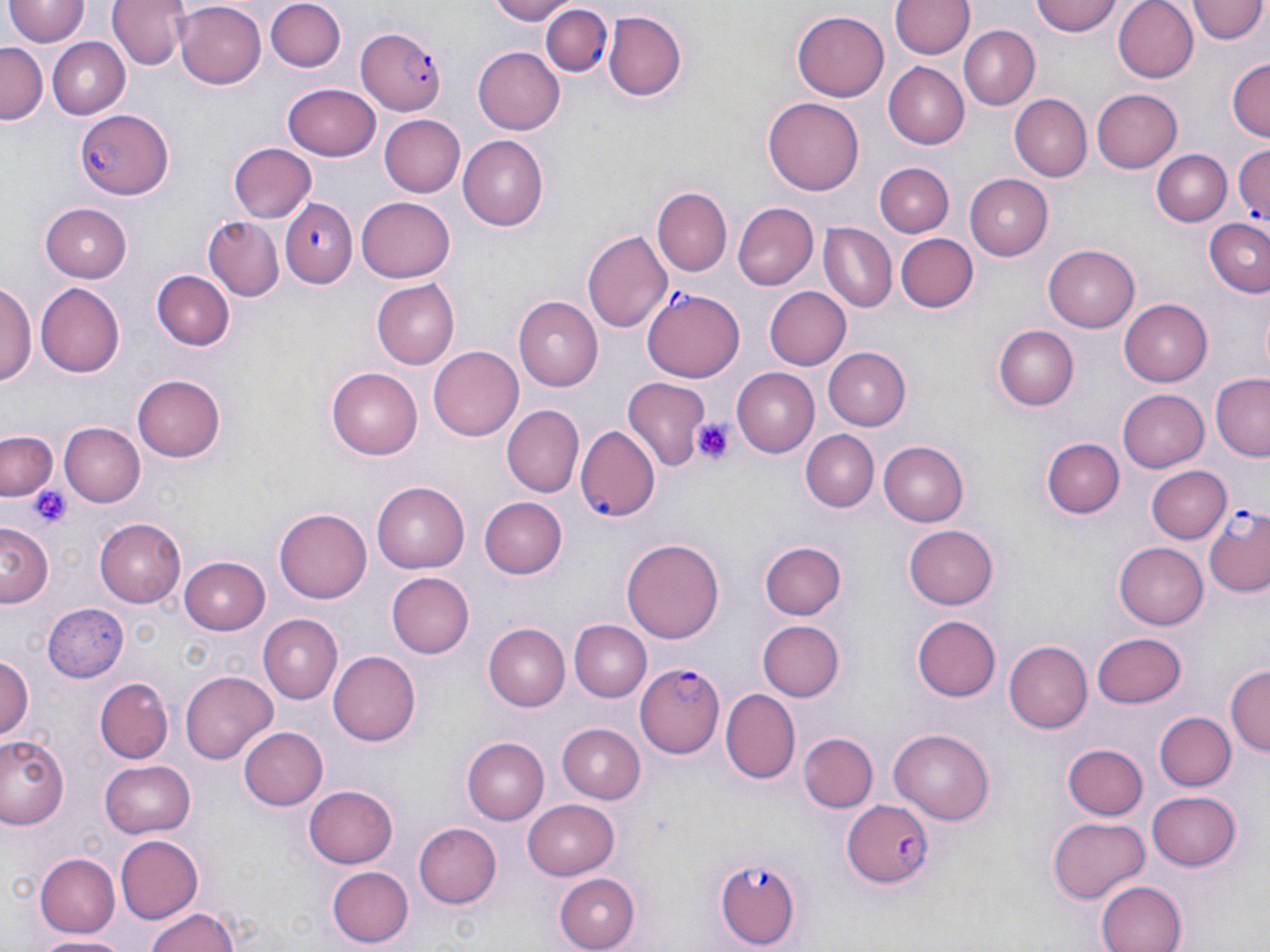

Summary:
  - Coordinate format: approximate bounding boxes as (x1, y1, x2, y2) in pixels
  - Uninfected red blood cell locations: (5, 0, 88, 47), (108, 0, 189, 69), (486, 0, 578, 24), (893, 0, 973, 60), (1030, 0, 1123, 37), (1111, 0, 1198, 83), (174, 2, 267, 88), (267, 2, 342, 73), (1189, 2, 1268, 47), (794, 8, 892, 102), (602, 10, 685, 102), (960, 27, 1039, 110), (46, 36, 129, 117), (0, 43, 46, 123), (472, 46, 565, 134), (1227, 58, 1268, 142), (882, 62, 970, 148), (283, 82, 381, 159), (1092, 89, 1183, 173), (1012, 94, 1093, 180), (763, 97, 865, 195), (377, 114, 464, 197), (457, 136, 550, 231), (229, 142, 318, 223), (1153, 150, 1231, 227), (875, 161, 953, 237), (962, 174, 1053, 259), (652, 186, 732, 276), (357, 194, 456, 281), (42, 202, 134, 280), (733, 202, 818, 289), (1203, 217, 1270, 296), (204, 218, 284, 302), (821, 223, 896, 311), (583, 230, 672, 336), (896, 234, 978, 312), (1044, 246, 1139, 332), (156, 270, 233, 349), (375, 279, 461, 369), (35, 283, 126, 377), (1, 284, 36, 388), (763, 287, 850, 371), (517, 296, 604, 391), (1119, 298, 1212, 385), (994, 325, 1079, 411), (428, 346, 526, 441), (822, 347, 910, 430), (326, 368, 423, 457), (732, 369, 820, 457), (133, 375, 227, 461), (1211, 376, 1269, 460), (624, 379, 710, 472), (1118, 389, 1210, 472), (504, 406, 582, 497), (59, 422, 145, 507), (800, 431, 877, 511), (0, 433, 57, 499), (1043, 437, 1123, 518), (879, 440, 968, 527), (1145, 466, 1230, 544), (373, 480, 470, 573), (480, 496, 569, 579), (275, 507, 372, 601), (96, 518, 188, 607), (2, 525, 51, 609), (903, 525, 999, 609), (621, 537, 726, 644), (759, 540, 846, 620), (1115, 544, 1208, 629), (179, 556, 270, 634), (388, 572, 475, 657), (44, 603, 127, 681), (259, 615, 342, 703), (912, 615, 1001, 702), (756, 619, 844, 702), (568, 620, 651, 702), (484, 624, 570, 710), (1093, 632, 1187, 708), (1006, 639, 1097, 734), (328, 651, 420, 745), (0, 654, 34, 742), (1225, 665, 1269, 759), (180, 671, 277, 763), (96, 676, 173, 762), (722, 688, 800, 784), (1156, 711, 1235, 791), (556, 723, 645, 806), (237, 725, 328, 811), (889, 729, 994, 824), (0, 733, 70, 831), (798, 733, 876, 814), (462, 737, 550, 824), (1063, 743, 1148, 820), (102, 760, 196, 837), (303, 785, 400, 868), (1149, 790, 1243, 869), (523, 799, 619, 878), (1047, 815, 1151, 903), (411, 821, 502, 911), (114, 834, 202, 925), (34, 853, 120, 937), (327, 866, 413, 948), (552, 871, 640, 951), (1093, 878, 1187, 952), (144, 908, 243, 952), (38, 933, 134, 951)
  - Platelet locations: (693, 417, 738, 466), (32, 484, 73, 530)
  - Plasmodium falciparum-infected red blood cell locations: (541, 5, 613, 78), (356, 28, 447, 113), (77, 108, 171, 199), (1234, 142, 1269, 232), (282, 198, 357, 289), (641, 289, 745, 382), (577, 427, 659, 522), (1203, 505, 1270, 598), (636, 660, 739, 757), (842, 799, 936, 888), (715, 856, 801, 950)
  - Slide-level diagnosis: Plasmodium falciparum
  - Stain: May-Grünwald-Giemsa
  - Image size: 1270×952 pixels
  - Field of view: one of a larger specimen
  - Magnification: 1000x
  - Preparation: thin blood film
  - Modality: optical microscopy